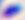
Summary:
  - Magnification: 400x
  - Identification: Toxoplasma gondii
  - Modality: micrograph